Give the extent of all uninfected red blood cells.
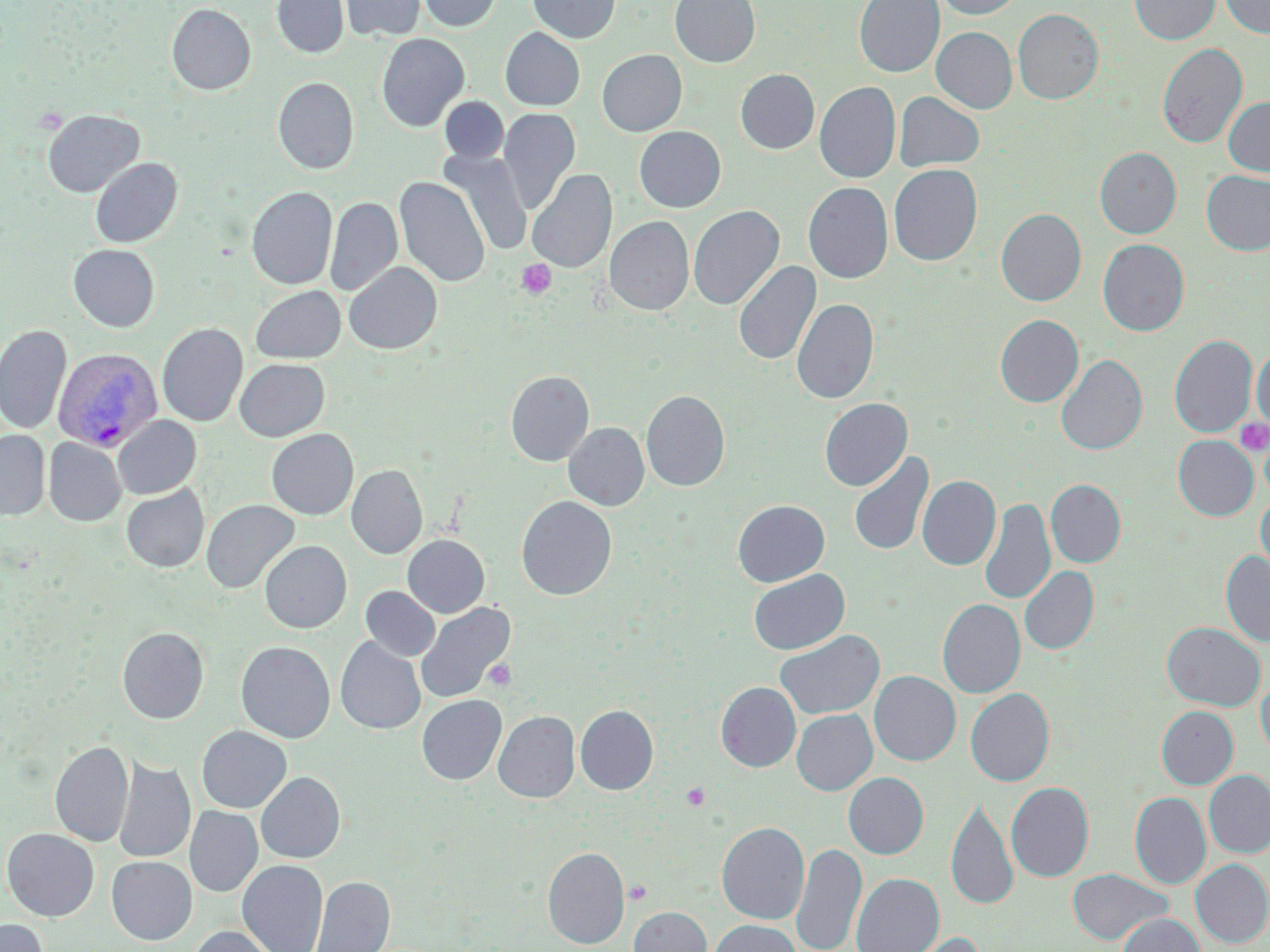
Approximate bounding boxes as (x1, y1, x2, y2) in pixels.
Uninfected red blood cells: (272, 0, 349, 58), (339, 0, 426, 41), (417, 0, 501, 32), (527, 0, 621, 43), (670, 0, 760, 67), (854, 0, 944, 77), (934, 0, 1025, 19), (1129, 0, 1220, 45), (1220, 0, 1270, 38), (167, 4, 256, 95), (1013, 9, 1103, 104), (501, 27, 585, 110), (931, 27, 1017, 113), (376, 32, 470, 132), (1157, 43, 1247, 148), (597, 49, 686, 136), (735, 69, 820, 154), (273, 77, 359, 174), (814, 82, 901, 183), (893, 91, 985, 172), (439, 96, 509, 165), (1223, 96, 1270, 177), (498, 107, 581, 213), (42, 109, 145, 198), (634, 126, 726, 212), (1095, 147, 1182, 239), (441, 150, 533, 255), (90, 157, 182, 248), (888, 164, 982, 266), (527, 170, 616, 273), (1201, 170, 1270, 256), (394, 177, 490, 288), (803, 182, 893, 284), (247, 186, 337, 290), (325, 196, 402, 297), (688, 205, 785, 311), (996, 208, 1087, 306), (604, 216, 694, 316), (1098, 239, 1189, 336), (68, 244, 160, 331), (733, 260, 821, 367), (344, 262, 442, 354), (250, 285, 346, 364), (791, 298, 878, 404), (995, 315, 1084, 407), (157, 323, 248, 427), (0, 324, 71, 435), (1169, 334, 1257, 439), (1251, 343, 1270, 435), (1056, 354, 1147, 456), (234, 358, 330, 441), (505, 370, 594, 466), (641, 390, 730, 491), (819, 398, 912, 491), (112, 416, 201, 499), (564, 422, 649, 510), (266, 428, 359, 520), (0, 430, 50, 520), (1172, 435, 1258, 520), (43, 438, 126, 526), (849, 450, 934, 556), (346, 464, 427, 559), (917, 475, 1000, 570), (1046, 479, 1126, 568), (121, 484, 209, 572), (1256, 491, 1270, 579), (516, 496, 617, 600), (979, 498, 1055, 605), (201, 500, 300, 594), (732, 500, 830, 587), (402, 535, 489, 618), (260, 540, 352, 633), (1220, 550, 1270, 648), (1019, 566, 1098, 655), (748, 569, 850, 655), (361, 586, 441, 661), (938, 598, 1025, 698), (415, 601, 515, 704), (1162, 622, 1265, 711), (117, 627, 209, 724), (774, 629, 885, 720), (335, 637, 426, 734), (235, 641, 335, 743), (870, 671, 961, 765), (1256, 676, 1270, 761), (716, 682, 801, 772), (965, 688, 1054, 786), (416, 695, 507, 785), (575, 705, 658, 794), (1156, 706, 1238, 789), (791, 709, 877, 795), (493, 711, 580, 802), (196, 726, 291, 813), (49, 741, 134, 847), (112, 759, 195, 864), (1203, 770, 1270, 859), (256, 772, 345, 863), (843, 772, 929, 858), (1006, 782, 1094, 882), (1130, 792, 1211, 888), (946, 796, 1017, 911), (184, 806, 263, 897), (716, 822, 809, 924), (2, 828, 99, 921), (792, 842, 867, 952), (542, 846, 629, 949), (106, 856, 197, 944), (1190, 859, 1270, 948), (237, 860, 328, 952), (1067, 869, 1174, 946), (852, 873, 944, 952), (311, 876, 395, 952), (629, 906, 712, 952), (1117, 913, 1205, 952), (0, 918, 48, 952), (709, 919, 801, 952), (189, 925, 281, 952), (898, 931, 987, 952).

Summary:
  - Plasmodium vivax-infected red blood cell locations: (52, 346, 163, 452)
  - Platelet locations: (516, 259, 556, 299), (1234, 418, 1269, 456), (484, 659, 517, 691), (681, 782, 710, 810), (625, 880, 651, 904)
  - Slide-level diagnosis: Plasmodium vivax
  - Modality: light microscopy
  - Preparation: thin blood film
  - Image size: 1270×952 pixels
  - Stain: May-Grünwald-Giemsa
  - Field of view: one of a larger specimen
  - Magnification: 1000x